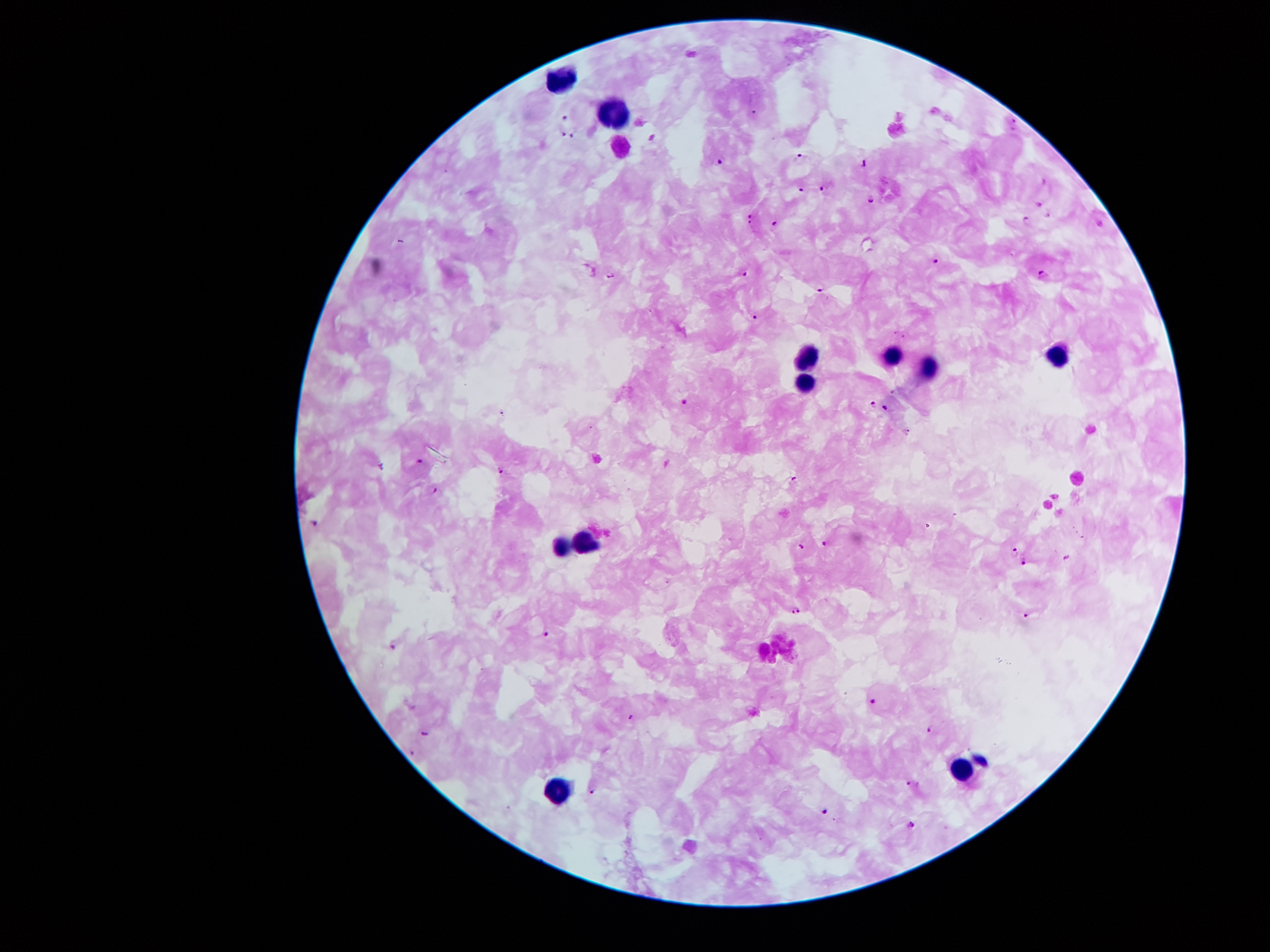
Approximate object centers, in pixels from the top-left corner.
Summary:
  - Plasmodium parasite locations: (x=566, y=119), (x=1016, y=123), (x=562, y=133), (x=571, y=137), (x=800, y=154), (x=721, y=161), (x=864, y=162), (x=822, y=187), (x=801, y=191), (x=872, y=200), (x=1039, y=204), (x=1047, y=215), (x=750, y=219), (x=1026, y=220), (x=775, y=223), (x=936, y=260), (x=744, y=272), (x=611, y=275), (x=1043, y=275), (x=823, y=290), (x=756, y=315), (x=895, y=333), (x=903, y=336), (x=685, y=402), (x=874, y=403), (x=885, y=407), (x=909, y=431), (x=421, y=460), (x=502, y=469), (x=795, y=477), (x=437, y=490), (x=317, y=521), (x=802, y=544), (x=825, y=544), (x=1016, y=550), (x=1068, y=557), (x=1025, y=563), (x=797, y=613), (x=1024, y=617), (x=545, y=633), (x=392, y=647), (x=871, y=702), (x=631, y=716), (x=425, y=730), (x=928, y=730), (x=414, y=754), (x=908, y=783), (x=594, y=791), (x=826, y=811), (x=912, y=824)
  - Leukocyte locations: (x=562, y=79), (x=616, y=113), (x=805, y=357), (x=893, y=357), (x=1060, y=362), (x=932, y=370), (x=805, y=383), (x=586, y=541), (x=564, y=546), (x=961, y=767), (x=559, y=790)
  - Capture: smartphone through the microscope eyepiece
  - Field of view: single
  - Preparation: thick blood smear
  - Image size: 1270×952 pixels
  - Magnification: 100x
  - Patient malaria status: infected with Plasmodium falciparum
  - Stain: Giemsa